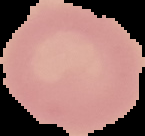
Summary:
  - Image type: segmented cell region with the area outside set to black
  - Preparation: thin blood smear
  - Malaria status: uninfected
  - Image size: 145×136 pixels